Locate every Plasmodium parasite.
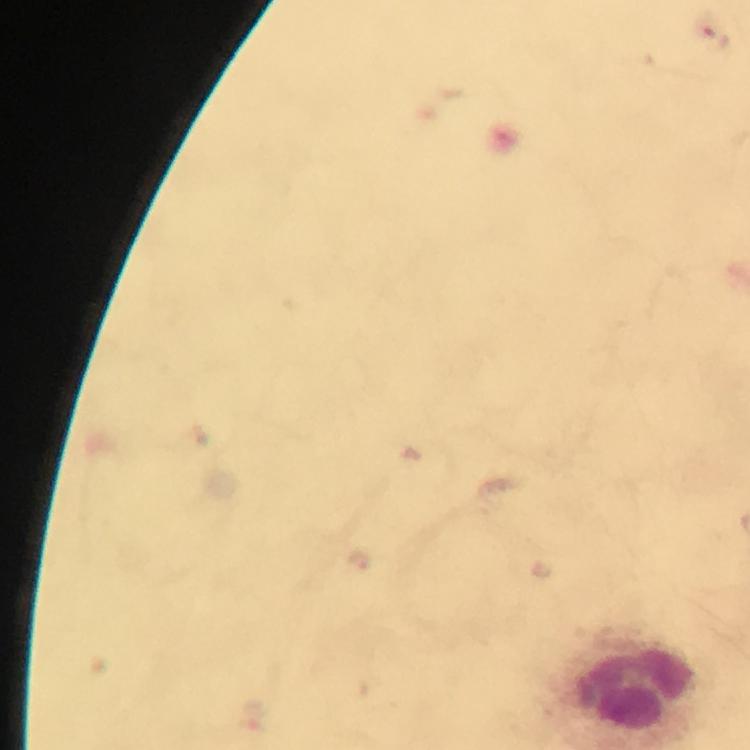
Approximate centers as (x, y) in pixels.
Plasmodium parasites: (716, 33).

Immersion oil was used. Image is 750×750 pixels. At 100x magnification. A crop from one field of view. Smartphone photograph taken through a microscope. Thick blood smear. From a diagnostic examination for malaria. Giemsa stain.